Evaluate for malaria.
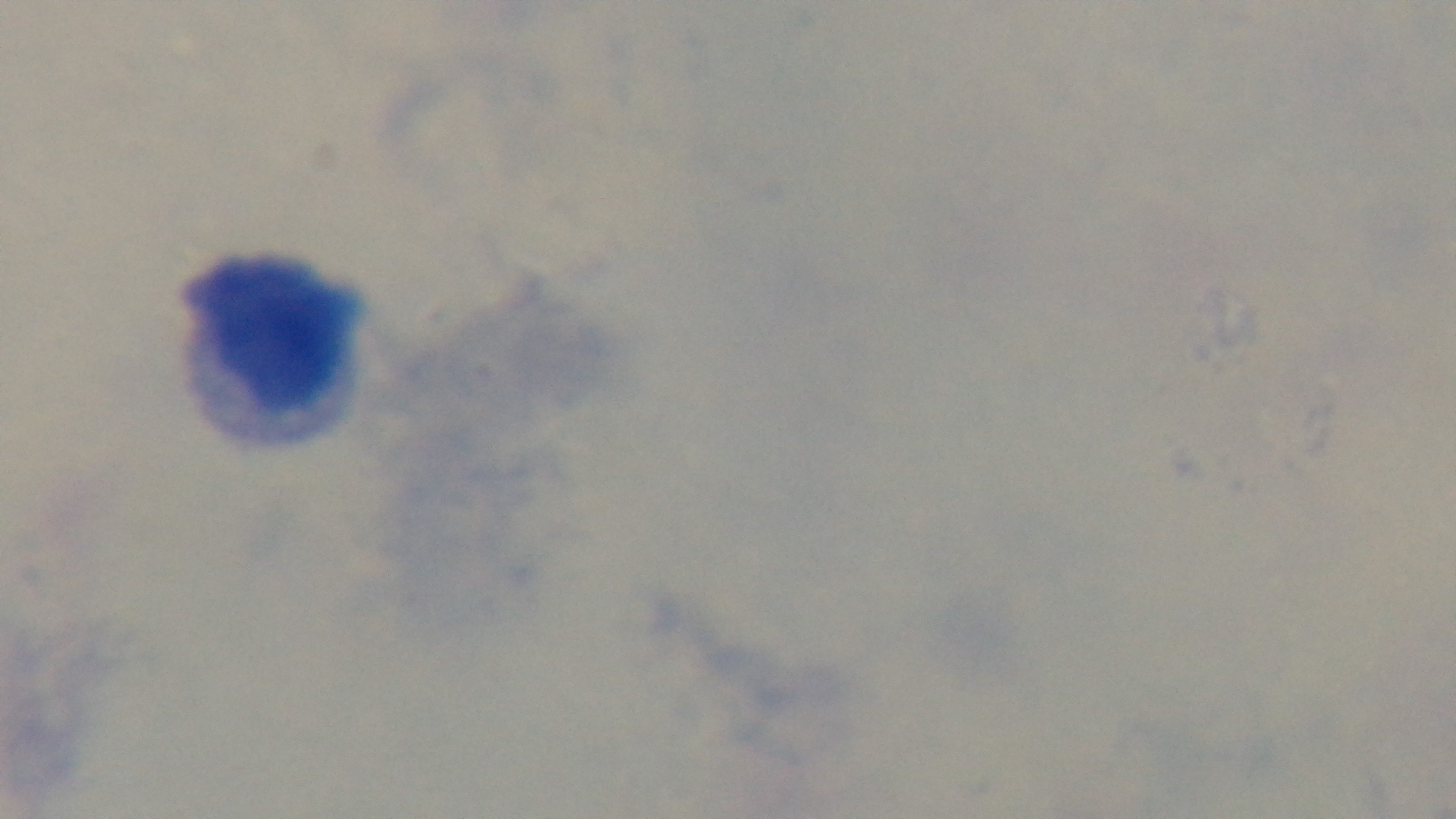

Uninfected.

Summary:
  - Objective: 100x oil immersion
  - Capture: mounted 4K digital camera
  - Preparation: thick smear
  - Stain: Giemsa
  - Modality: light microscopy
  - Field of view: single